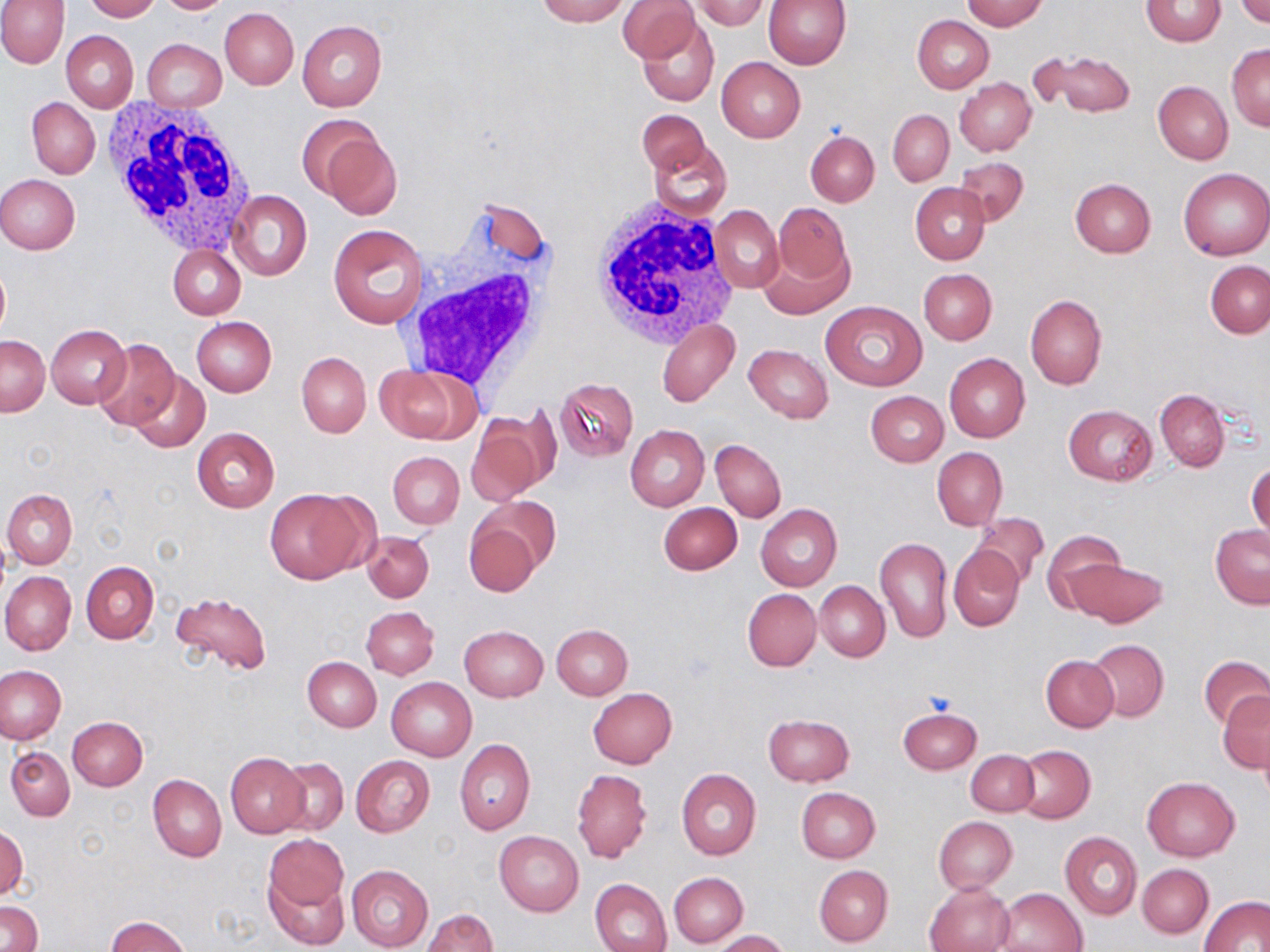

slide-level diagnosis = no evidence of blood parasites
platelet locations = approximate bounding boxes as [x1, y1, x2, y2] in pixels: [921, 689, 960, 719]
preparation = thin blood smear
image size = 1270×952 pixels
magnification = 1000x
field of view = single
white blood cell locations = approximate bounding boxes as [x1, y1, x2, y2] in pixels: [102, 100, 257, 256], [588, 199, 741, 352], [394, 206, 560, 396]
stain = May-Grünwald-Giemsa
modality = optical microscopy
uninfected red blood cell locations = approximate bounding boxes as [x1, y1, x2, y2] in pixels: [84, 0, 160, 22], [155, 0, 235, 14], [535, 0, 629, 26], [761, 0, 850, 70], [959, 0, 1048, 30], [1141, 0, 1225, 47], [1235, 0, 1269, 26], [0, 1, 68, 68], [618, 1, 699, 62], [691, 1, 771, 31], [220, 7, 299, 89], [912, 15, 993, 93], [637, 17, 718, 107], [297, 20, 387, 112], [62, 31, 138, 112], [142, 39, 226, 111], [1227, 43, 1270, 130], [1041, 51, 1134, 117], [716, 57, 806, 142], [956, 77, 1036, 155], [1153, 82, 1233, 164], [28, 98, 100, 179], [637, 109, 709, 178], [888, 110, 954, 185], [313, 124, 402, 219], [806, 131, 879, 207], [649, 139, 732, 221], [952, 157, 1029, 226], [1178, 168, 1269, 261], [0, 175, 80, 254], [1071, 179, 1156, 257], [909, 183, 989, 265], [229, 190, 312, 280], [773, 202, 851, 286], [711, 205, 783, 294], [328, 225, 428, 328], [760, 243, 850, 319], [168, 245, 245, 319], [1205, 259, 1270, 338], [0, 264, 10, 342], [918, 268, 996, 345], [1026, 295, 1107, 390], [822, 299, 927, 390], [192, 317, 276, 397], [657, 317, 739, 408], [47, 325, 131, 410], [0, 335, 49, 415], [92, 338, 181, 431], [744, 344, 832, 423], [297, 352, 371, 437], [944, 353, 1030, 442], [376, 365, 472, 442], [128, 370, 209, 453], [555, 378, 638, 461], [1155, 389, 1229, 471], [866, 390, 948, 467], [1065, 404, 1156, 484], [466, 416, 551, 507], [625, 425, 710, 511], [191, 428, 279, 512], [711, 439, 786, 523], [932, 447, 1007, 530], [387, 451, 463, 529], [1248, 461, 1269, 547], [3, 489, 77, 569], [264, 489, 369, 584], [659, 502, 742, 575], [755, 503, 842, 591], [972, 512, 1048, 587], [463, 519, 542, 597], [1209, 525, 1270, 608], [362, 531, 434, 602], [1042, 531, 1125, 615], [875, 538, 952, 643], [949, 546, 1025, 630], [1064, 558, 1166, 628], [81, 560, 160, 643], [1, 571, 76, 655], [815, 581, 890, 662], [743, 588, 821, 670], [171, 590, 273, 677], [360, 606, 440, 679], [550, 624, 633, 699], [459, 625, 548, 701], [1088, 639, 1169, 722], [1041, 655, 1118, 732], [1200, 655, 1270, 730], [302, 657, 381, 731], [0, 665, 66, 744], [387, 677, 476, 760], [588, 687, 677, 769], [1219, 692, 1270, 769], [897, 707, 981, 773], [763, 714, 855, 786], [67, 716, 147, 790], [455, 740, 535, 835], [1014, 744, 1095, 823], [6, 746, 74, 821], [966, 750, 1039, 817], [225, 752, 309, 837], [351, 756, 434, 836], [273, 757, 349, 836], [572, 767, 652, 864], [676, 769, 760, 860], [147, 774, 226, 862], [1143, 777, 1239, 861], [796, 787, 880, 862], [933, 816, 1017, 892], [1, 826, 26, 901], [495, 831, 584, 915], [1060, 832, 1142, 921], [263, 834, 349, 916], [1138, 864, 1212, 937], [346, 865, 433, 951], [814, 865, 893, 947], [264, 869, 348, 949], [670, 872, 748, 947], [590, 877, 671, 952], [925, 881, 1016, 952], [996, 887, 1088, 952], [1202, 895, 1268, 952], [0, 902, 43, 952], [421, 909, 497, 952], [105, 916, 192, 952], [713, 930, 789, 952]